Assess this cell for malaria.
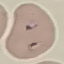

It is parasitized.

Summary:
  - Capture: smartphone through the microscope eyepiece
  - Preparation: thin blood smear
  - Stain: Giemsa
  - Image type: cell patch, automatically extracted from a larger field of view and resized to 64 × 64 pixels